Classify this cell by malaria status.
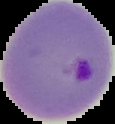
It is parasitized.

image size = 115×124 pixels
preparation = thin blood film
image type = segmented cell region on a black background